Locate every blood parasite and identify its species.
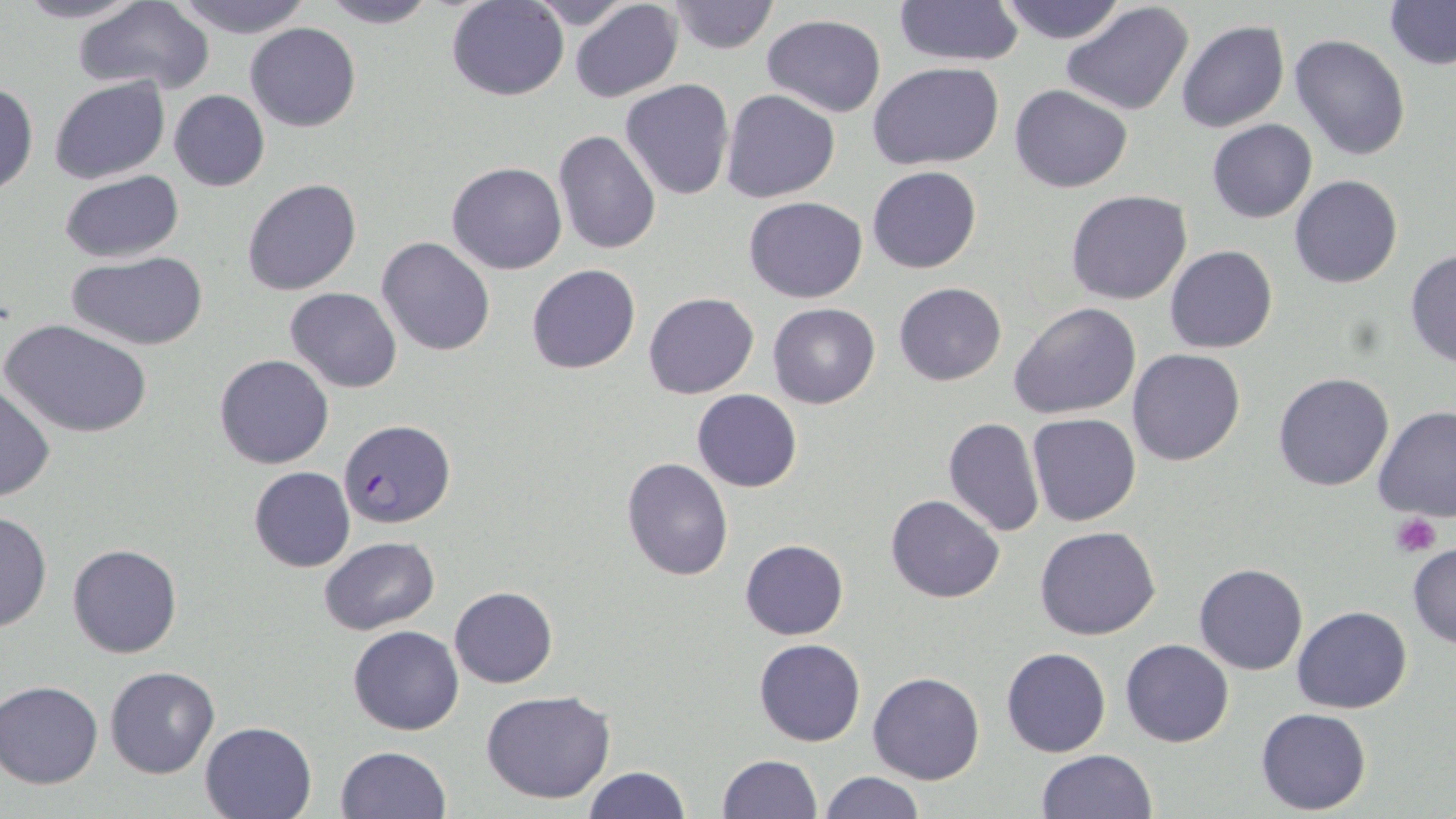
Approximate bounding boxes as (x1, y1, x2, y2) in pixels.
Plasmodium falciparum-infected red blood cells: (338, 420, 453, 529).
No Plasmodium ovale, Plasmodium malariae, Plasmodium vivax, Babesia divergens, or Trypanosoma brucei observed.

Summary:
  - Platelet locations: (1390, 512, 1443, 558)
  - Uninfected red blood cell locations: (10, 0, 150, 24), (168, 0, 314, 39), (315, 0, 439, 29), (523, 0, 644, 30), (894, 0, 1024, 68), (995, 0, 1130, 44), (71, 1, 216, 96), (446, 1, 567, 101), (667, 1, 778, 53), (1060, 1, 1195, 117), (1383, 1, 1456, 69), (569, 2, 683, 103), (760, 15, 886, 118), (1176, 20, 1288, 134), (244, 22, 361, 132), (1289, 34, 1411, 161), (869, 62, 1004, 167), (49, 77, 170, 186), (619, 79, 735, 201), (1, 82, 38, 197), (1009, 85, 1132, 194), (719, 89, 840, 204), (169, 90, 269, 191), (1206, 119, 1317, 223), (552, 129, 662, 257), (446, 162, 567, 275), (867, 166, 981, 273), (57, 170, 182, 264), (1290, 175, 1402, 289), (240, 177, 362, 296), (1065, 189, 1192, 305), (743, 196, 868, 304), (376, 236, 496, 357), (1164, 246, 1278, 354), (1404, 249, 1456, 368), (64, 252, 209, 350), (527, 263, 640, 375), (894, 282, 1007, 385), (285, 287, 402, 393), (642, 291, 759, 399), (1010, 301, 1142, 421), (767, 302, 880, 408), (4, 318, 154, 440), (1127, 348, 1246, 466), (214, 354, 334, 468), (1273, 372, 1394, 492), (0, 383, 55, 503), (690, 389, 803, 492), (1371, 404, 1456, 520), (1027, 413, 1142, 526), (942, 418, 1045, 537), (621, 457, 733, 581), (249, 466, 355, 572), (885, 495, 1004, 603), (0, 511, 52, 631), (1035, 525, 1161, 640), (318, 536, 439, 636), (740, 539, 849, 640), (1407, 542, 1456, 650), (68, 544, 182, 658), (1194, 563, 1307, 675), (448, 586, 558, 687), (1291, 605, 1413, 713), (349, 625, 463, 735), (754, 638, 866, 747), (1121, 638, 1234, 747), (1001, 647, 1111, 758), (105, 666, 220, 779), (868, 673, 984, 785), (0, 681, 103, 788), (481, 689, 618, 805), (1256, 707, 1371, 814), (200, 721, 318, 818), (336, 744, 451, 818), (1035, 749, 1160, 818), (718, 755, 821, 818), (581, 766, 690, 819), (818, 772, 926, 818)
  - Slide-level diagnosis: Plasmodium falciparum
  - Field of view: one of a larger specimen
  - Magnification: 1000x
  - Stain: May-Grünwald-Giemsa
  - Preparation: thin blood smear
  - Image size: 1456×819 pixels
  - Modality: light microscopy